Describe the morphology of the erythrocytes.
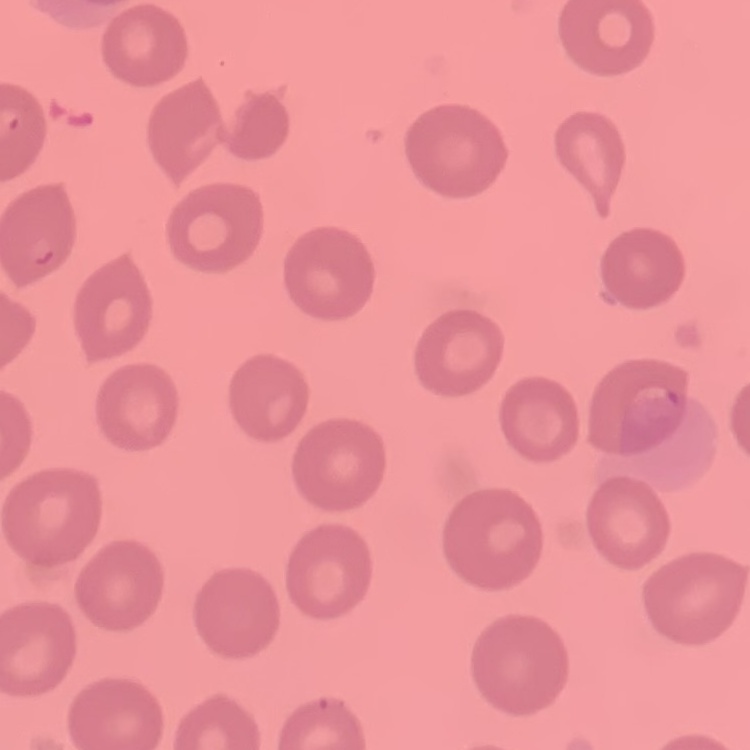

They show no rouleaux formation.

Summary:
  - Preparation: thin peripheral smear
  - Stain: Field's or Giemsa
  - Image type: square crop of a larger photomicrograph